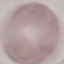
Summary:
  - Result: no malaria parasites seen
  - Stain: Giemsa
  - Image type: automatically extracted cell patch, resized to 64 × 64 pixels
  - Preparation: thin smear
  - Capture: smartphone camera at the microscope eyepiece